Describe the morphology of the erythrocytes.
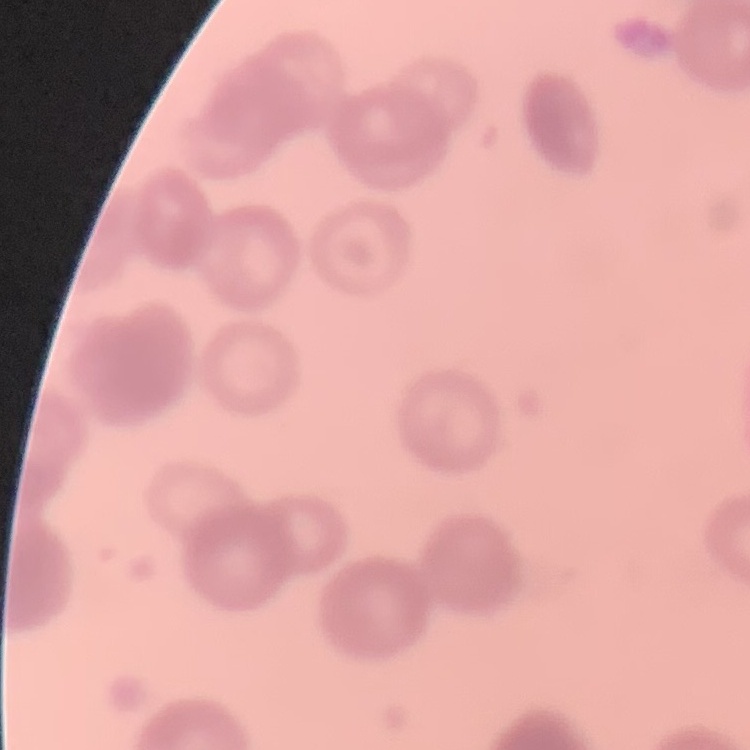

Rouleaux formation.

Summary:
  - Image type: one tile cut from a larger photomicrograph
  - Preparation: thin blood smear
  - Stain: Field's or Giemsa